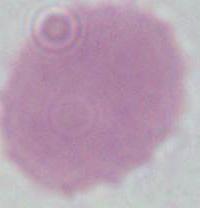
Summary:
  - Modality: micrograph
  - Identification: red blood cell
  - Magnification: 1000x